Name the parasite shown.
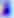

Toxoplasma gondii.

magnification = 400x
modality = photomicrograph